Assess the morphology of the erythrocytes.
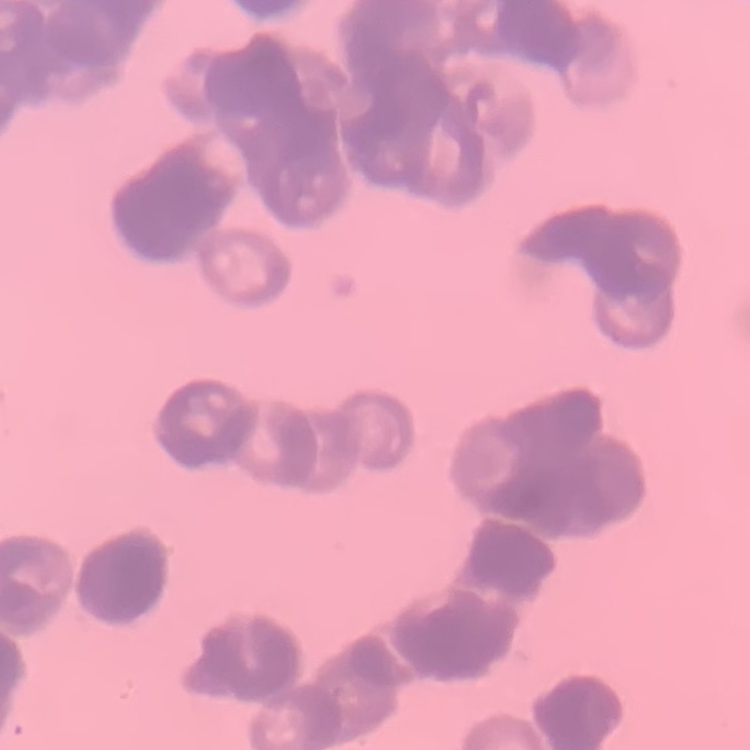
They show rouleaux formation.

Summary:
  - Preparation: thin peripheral smear
  - Stain: Field's or Giemsa
  - Image type: one tile cut from a larger photomicrograph